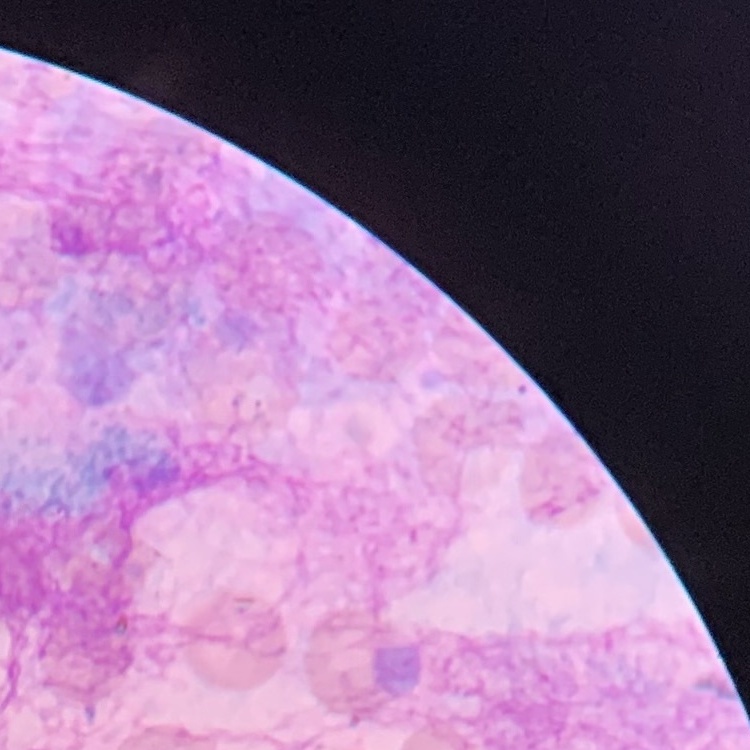

erythrocyte_morphology: no rouleaux formation
preparation: thin peripheral smear
stain: Field's or Giemsa
image_type: one tile cut from a larger photomicrograph